Give the preparation type.
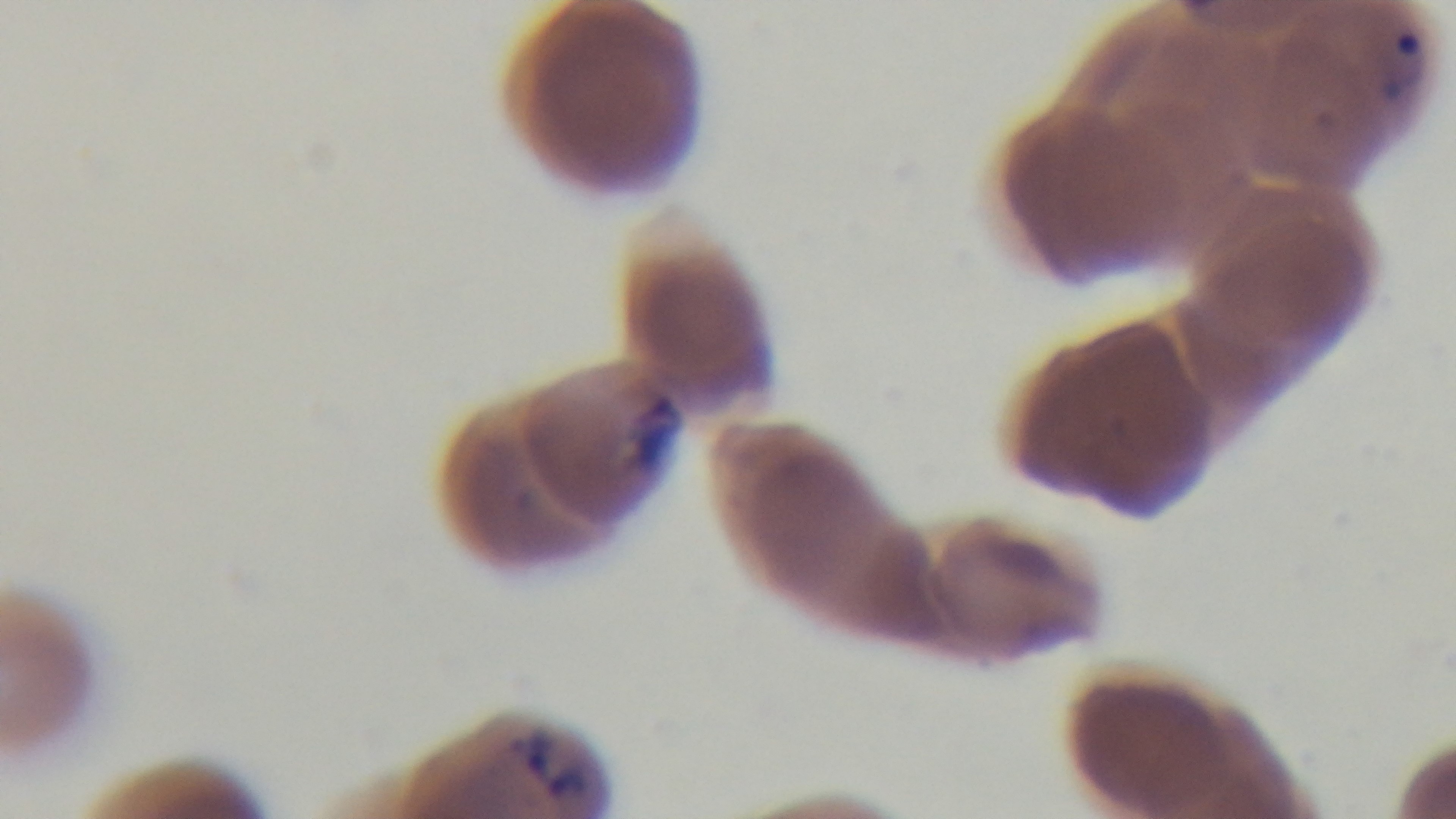
A thin smear.

capture = mounted 4K digital camera
stain = Giemsa
field of view = one from the slide
malaria status = infected
objective = 100x oil immersion
modality = light microscopy